Report the malaria status of this cell.
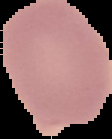

Uninfected.

image type = cell region segmented out of the field of view; surrounding area masked to black
preparation = thin blood film
image size = 112×139 pixels